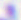

Summary:
  - Identification: Toxoplasma gondii
  - Modality: micrograph
  - Magnification: 400x